Comment on the morphology of the red blood cells.
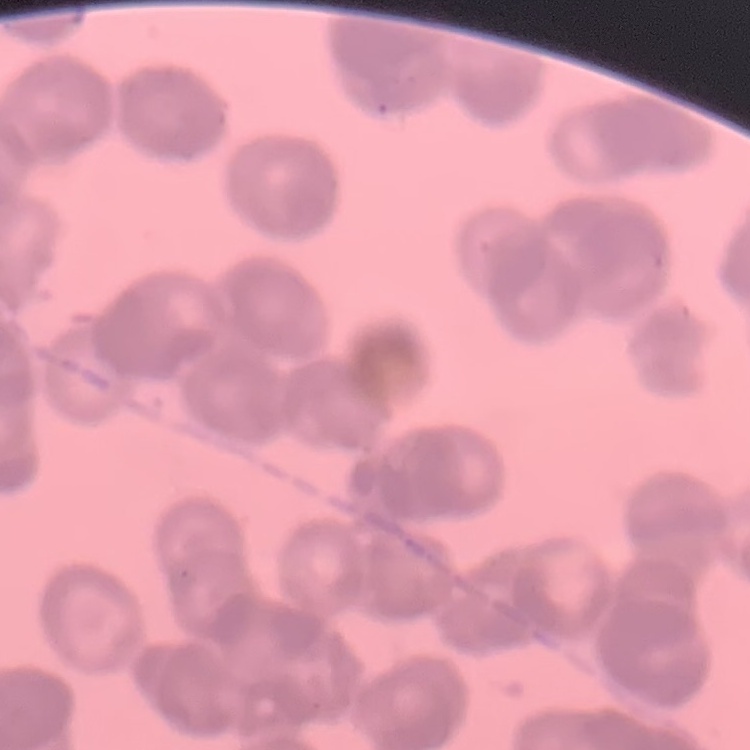

They show rouleaux formation.

Summary:
  - Image type: square crop of a larger photomicrograph
  - Preparation: thin peripheral smear
  - Stain: Field's or Giemsa